Outline each blood parasite and name the species.
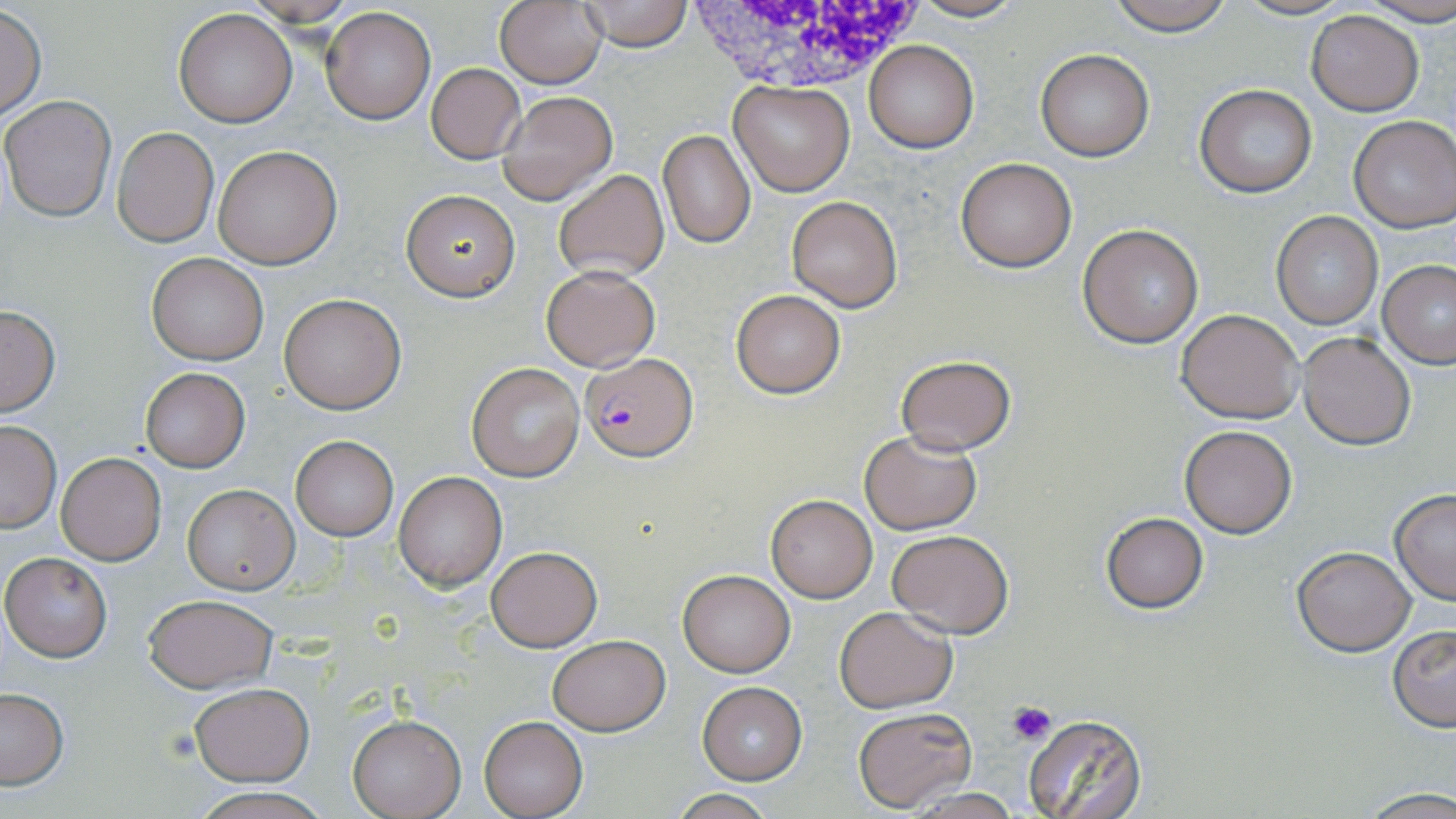

Approximate bounding boxes as (x1,y1)-(x2,y2) corner pairs in pixels.
Plasmodium falciparum-infected red blood cells: (581,350)-(698,461).
No Plasmodium ovale, Plasmodium malariae, Plasmodium vivax, Babesia divergens, or Trypanosoma brucei observed.

Summary:
  - White blood cell locations: (685,0)-(926,96)
  - Uninfected red blood cell locations: (577,0)-(693,50), (903,0)-(1030,23), (1104,0)-(1238,36), (1360,0)-(1456,27), (495,1)-(608,89), (1,5)-(46,122), (319,7)-(435,124), (173,9)-(297,127), (1307,9)-(1424,116), (863,40)-(978,152), (1036,50)-(1153,161), (427,64)-(526,162), (729,80)-(855,197), (1194,85)-(1317,198), (498,91)-(617,205), (1,95)-(116,221), (1349,115)-(1456,232), (112,128)-(218,247), (658,129)-(754,247), (213,146)-(341,268), (955,156)-(1077,272), (553,169)-(669,280), (402,190)-(518,300), (785,195)-(903,312), (1269,212)-(1383,329), (1078,224)-(1204,348), (146,252)-(270,366), (1379,259)-(1456,367), (541,265)-(660,371), (730,290)-(845,398), (279,293)-(406,413), (1,305)-(60,417), (1177,309)-(1305,423), (1296,331)-(1416,449), (894,355)-(1016,454), (465,362)-(585,482), (140,368)-(250,471), (0,420)-(61,533), (1180,425)-(1296,537), (858,430)-(982,534), (291,436)-(398,541), (56,453)-(167,566), (393,470)-(506,591), (183,484)-(297,594), (1389,490)-(1456,604), (766,495)-(878,602), (1099,510)-(1209,614), (887,528)-(1014,638), (485,544)-(603,652), (1291,546)-(1416,656), (1,552)-(112,661), (678,569)-(795,677), (142,594)-(276,692), (833,606)-(958,713), (1388,625)-(1456,731), (546,635)-(670,735), (697,681)-(807,783), (188,682)-(313,784), (0,689)-(68,789), (852,707)-(976,811), (1020,713)-(1149,819), (348,715)-(465,818), (479,716)-(587,818), (191,788)-(331,819), (1358,789)-(1456,818), (667,790)-(783,819)
  - Platelet locations: (1006,700)-(1058,746)
  - Slide-level diagnosis: Plasmodium falciparum
  - Modality: light microscopy
  - Image size: 1456×819 pixels
  - Stain: May-Grünwald-Giemsa
  - Field of view: one of a larger specimen
  - Preparation: thin blood smear
  - Magnification: 1000x